Identify the parasite.
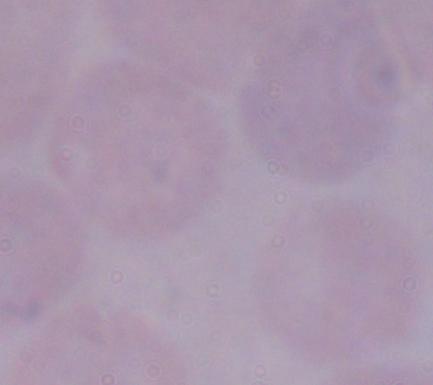

This is a trypanosome.

Photomicrograph. Captured at 1000x magnification.